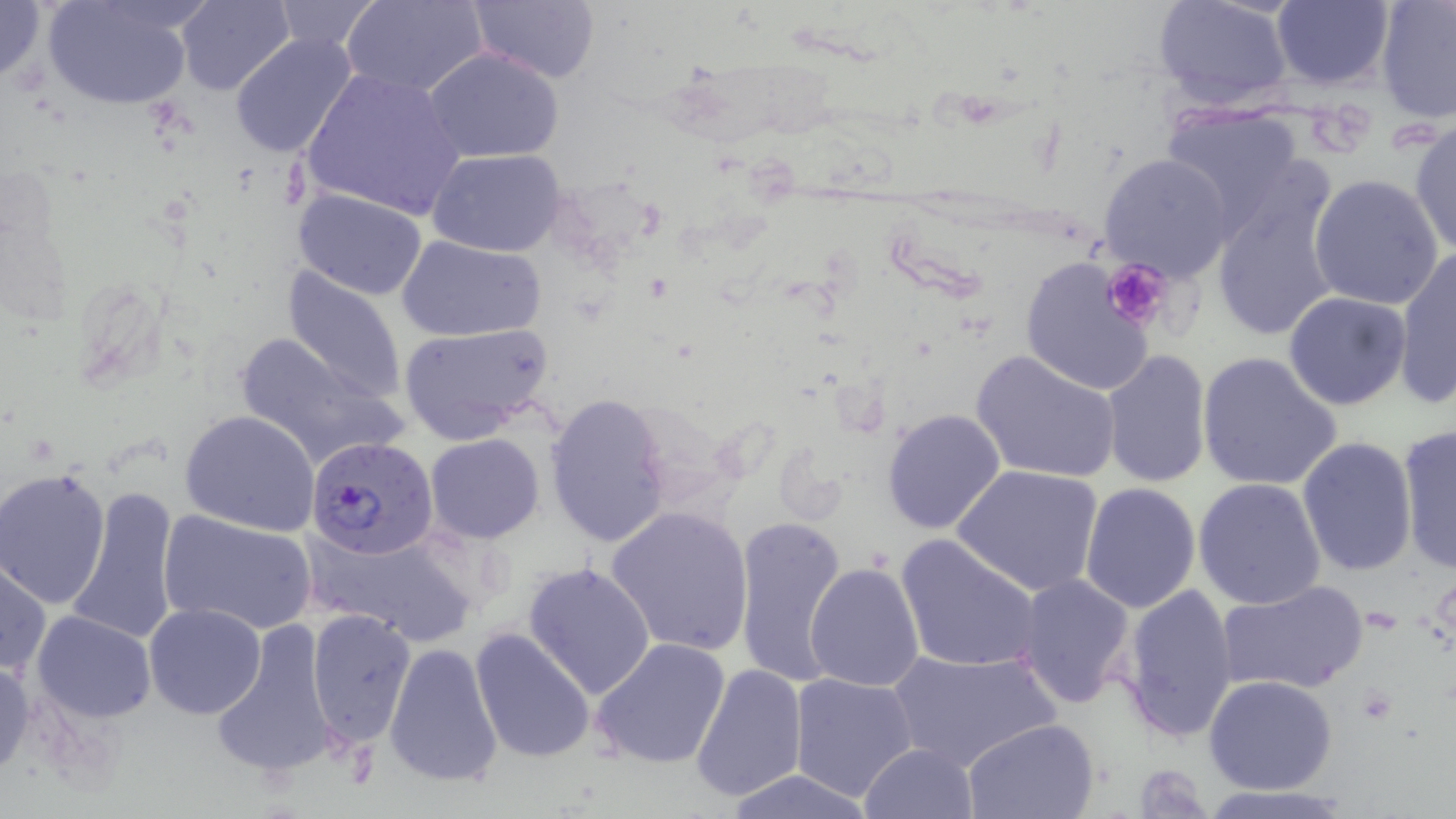

slide_level_diagnosis: Plasmodium falciparum
magnification: 1000x
stain: May-Grünwald-Giemsa
plasmodium_falciparum_infected_red_blood_cell_locations: 'approximate bounding boxes as (x1, y1, x2, y2) in pixels: (307, 437, 438, 560)'
uninfected_red_blood_cell_locations: 'approximate bounding boxes as (x1, y1, x2, y2) in pixels: (0, 0, 50, 92), (43, 0, 196, 110), (176, 0, 295, 95), (343, 0, 490, 98), (468, 0, 601, 85), (1152, 0, 1294, 112), (1376, 0, 1456, 124), (1269, 1, 1394, 89), (268, 2, 383, 56), (230, 33, 358, 158), (423, 47, 565, 164), (301, 65, 467, 225), (1157, 104, 1308, 235), (1407, 117, 1456, 258), (427, 149, 568, 257), (1098, 152, 1236, 283), (1207, 169, 1342, 343), (1309, 173, 1444, 308), (292, 186, 427, 300), (397, 233, 546, 342), (1394, 248, 1456, 408), (1020, 256, 1158, 397), (283, 266, 408, 403), (1283, 291, 1413, 411), (397, 322, 555, 445), (228, 327, 403, 471), (970, 348, 1122, 484), (1197, 350, 1342, 493), (1101, 351, 1213, 489), (543, 392, 673, 549), (881, 407, 1007, 536), (180, 410, 321, 535), (1399, 425, 1455, 571), (424, 434, 545, 543), (1297, 435, 1418, 577), (952, 463, 1105, 597), (0, 467, 112, 609), (1194, 477, 1327, 610), (1078, 481, 1201, 612), (66, 485, 182, 646), (605, 505, 753, 657), (161, 512, 316, 637), (733, 513, 851, 690), (306, 526, 479, 644), (895, 533, 1042, 674), (0, 559, 50, 678), (522, 560, 656, 701), (805, 560, 926, 691), (1013, 574, 1137, 711), (1218, 579, 1369, 696), (1118, 582, 1240, 743), (144, 603, 266, 719), (305, 606, 418, 748), (31, 610, 156, 722), (211, 618, 339, 782), (469, 627, 597, 764), (591, 637, 733, 771), (383, 640, 505, 789), (887, 647, 1057, 775), (0, 657, 34, 781), (691, 662, 808, 803), (789, 670, 920, 802), (1204, 674, 1337, 795), (962, 718, 1101, 818), (858, 742, 980, 819), (720, 769, 880, 818)'
image_size: 1456×819 pixels
modality: light microscopy
preparation: thin blood film
field_of_view: single
platelet_locations: 'approximate bounding boxes as (x1, y1, x2, y2) in pixels: (1102, 257, 1173, 331)'